Report the malaria status of this cell.
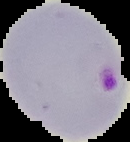
Parasitized.

image_type: segmented cell region with the area outside set to black
preparation: thin blood film
image_size: 130×142 pixels